Identify the parasite.
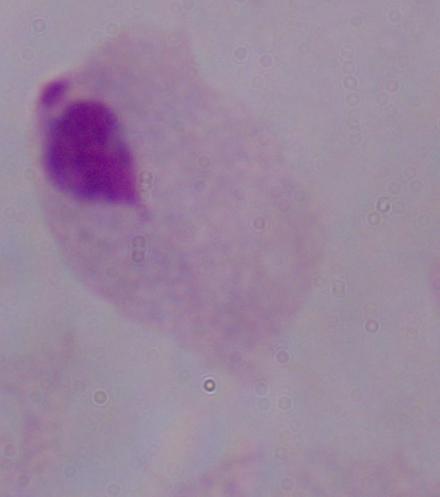

A trichomonad.

Summary:
  - Modality: micrograph
  - Magnification: 1000x